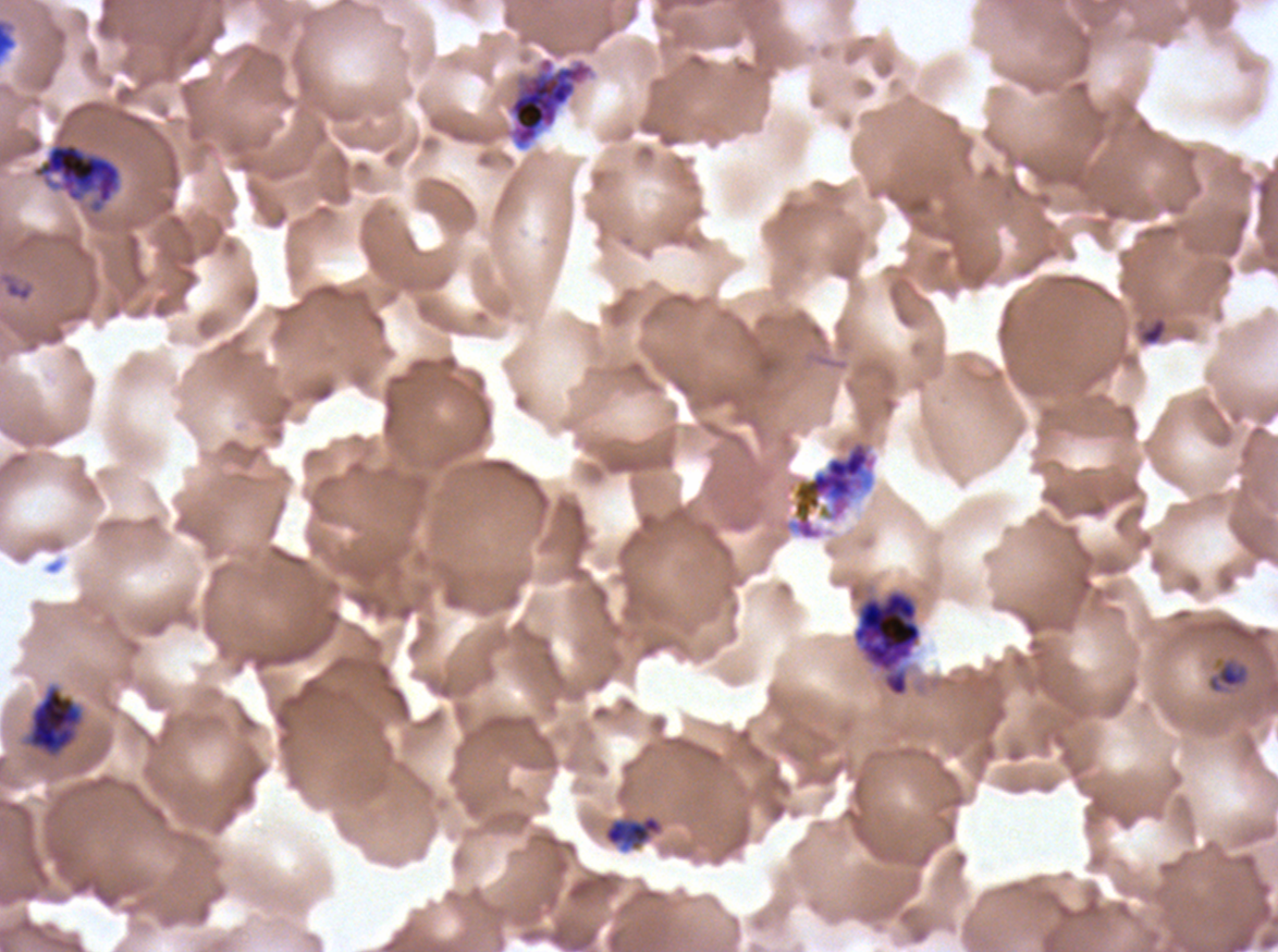
{
  "image_size": "1278×952 pixels",
  "stain": "Giemsa",
  "debris_locations": "approximate bounding boxes as [x1, y1, x2, y2] in pixels: [0, 18, 18, 61], [1137, 316, 1169, 347]",
  "late_schizont_locations": "approximate bounding boxes as [x1, y1, x2, y2] in pixels: [787, 438, 878, 541]",
  "life_cycle_stages_observed": "ring, late-ring/early-trophozoite, early schizont, late schizont",
  "preparation": "thin blood smear",
  "late_ring_early_trophozoite_locations": "approximate bounding boxes as [x1, y1, x2, y2] in pixels: [1206, 657, 1250, 695], [602, 813, 664, 853]",
  "ring_locations": "approximate bounding boxes as [x1, y1, x2, y2] in pixels: [0, 272, 34, 302]",
  "field_of_view": "sub-image separated from a larger composite",
  "early_schizont_locations": "approximate bounding boxes as [x1, y1, x2, y2] in pixels: [508, 56, 594, 149], [31, 141, 122, 214], [852, 589, 923, 697], [27, 686, 82, 756]",
  "specimen": "P. falciparum cultured ex vivo for 24 to 48 hours, from a patient in The Gambia"
}